State which parasite is depicted.
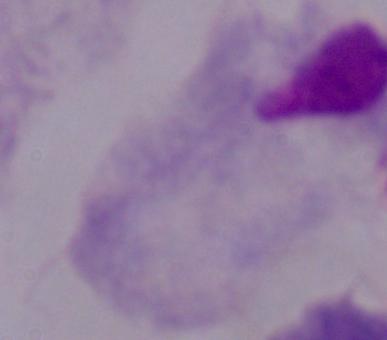
A trichomonad.

Summary:
  - Modality: photomicrograph
  - Magnification: 1000x